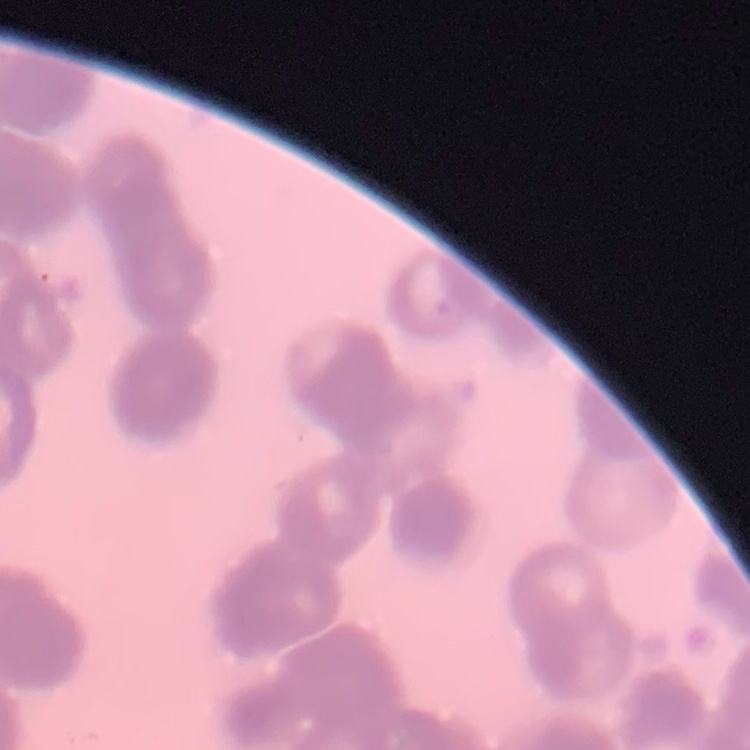 The red blood cells exhibit rouleaux formation. One tile cut from a larger photomicrograph. Stained with either Field's or Giemsa. Thin peripheral smear.